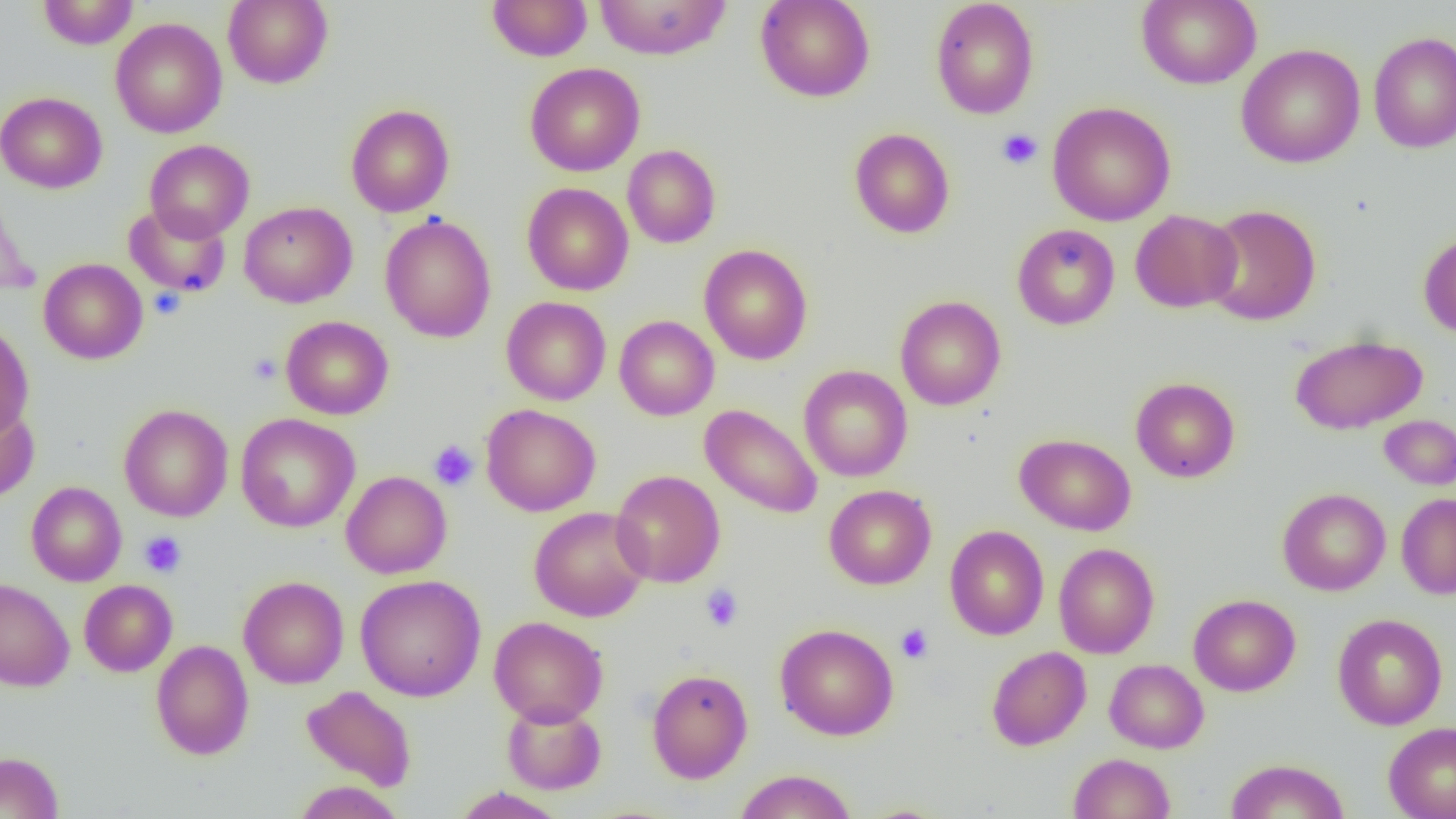

Summary:
  - Coordinate format: approximate bounding boxes as (x1, y1, x2, y2) in pixels
  - Platelet locations: (997, 129, 1042, 169), (149, 288, 185, 320), (249, 353, 282, 384), (429, 440, 478, 490), (139, 531, 187, 578), (700, 584, 744, 632), (895, 623, 934, 664)
  - Uninfected red blood cell locations: (37, 0, 139, 49), (223, 0, 333, 89), (487, 0, 592, 62), (594, 0, 732, 60), (755, 0, 875, 102), (930, 0, 1039, 119), (1136, 0, 1261, 89), (110, 17, 227, 139), (1368, 32, 1456, 153), (1236, 43, 1365, 168), (525, 62, 645, 176), (0, 91, 107, 193), (1048, 101, 1176, 226), (345, 104, 454, 217), (849, 128, 955, 238), (144, 140, 254, 242), (622, 144, 720, 248), (0, 179, 38, 300), (522, 182, 634, 296), (239, 202, 357, 308), (124, 203, 230, 298), (1202, 204, 1321, 326), (1130, 209, 1242, 313), (380, 214, 496, 343), (1012, 223, 1120, 330), (1418, 230, 1456, 338), (698, 244, 813, 365), (38, 258, 148, 364), (894, 295, 1006, 411), (501, 296, 612, 405), (614, 315, 719, 420), (280, 316, 394, 420), (0, 323, 34, 438), (1290, 334, 1428, 434), (798, 364, 912, 482), (1130, 377, 1240, 483), (0, 401, 39, 503), (119, 404, 233, 522), (481, 404, 601, 516), (700, 404, 823, 519), (235, 413, 361, 533), (1379, 415, 1456, 489), (1014, 433, 1136, 536), (348, 469, 460, 690), (611, 469, 725, 587), (341, 471, 452, 579), (26, 482, 127, 586), (823, 484, 936, 589), (1277, 488, 1391, 596), (1396, 493, 1456, 599), (529, 505, 651, 622), (945, 525, 1048, 640), (1054, 542, 1159, 658), (355, 574, 486, 701), (238, 576, 349, 689), (0, 579, 74, 691), (79, 579, 177, 677), (1188, 594, 1301, 696), (1333, 613, 1447, 730), (488, 616, 609, 727), (774, 623, 899, 741), (151, 639, 254, 760), (986, 646, 1091, 751), (1104, 659, 1209, 753), (646, 668, 753, 783), (302, 685, 416, 791), (502, 701, 607, 795), (1383, 722, 1456, 819), (0, 751, 64, 819), (1069, 753, 1175, 818), (1225, 758, 1350, 819), (733, 769, 857, 819), (294, 781, 405, 818), (452, 787, 567, 819)
  - Slide-level diagnosis: no evidence of blood parasites
  - Preparation: thin blood film
  - Field of view: single
  - Magnification: 1000x
  - Modality: light microscopy
  - Image size: 1456×819 pixels